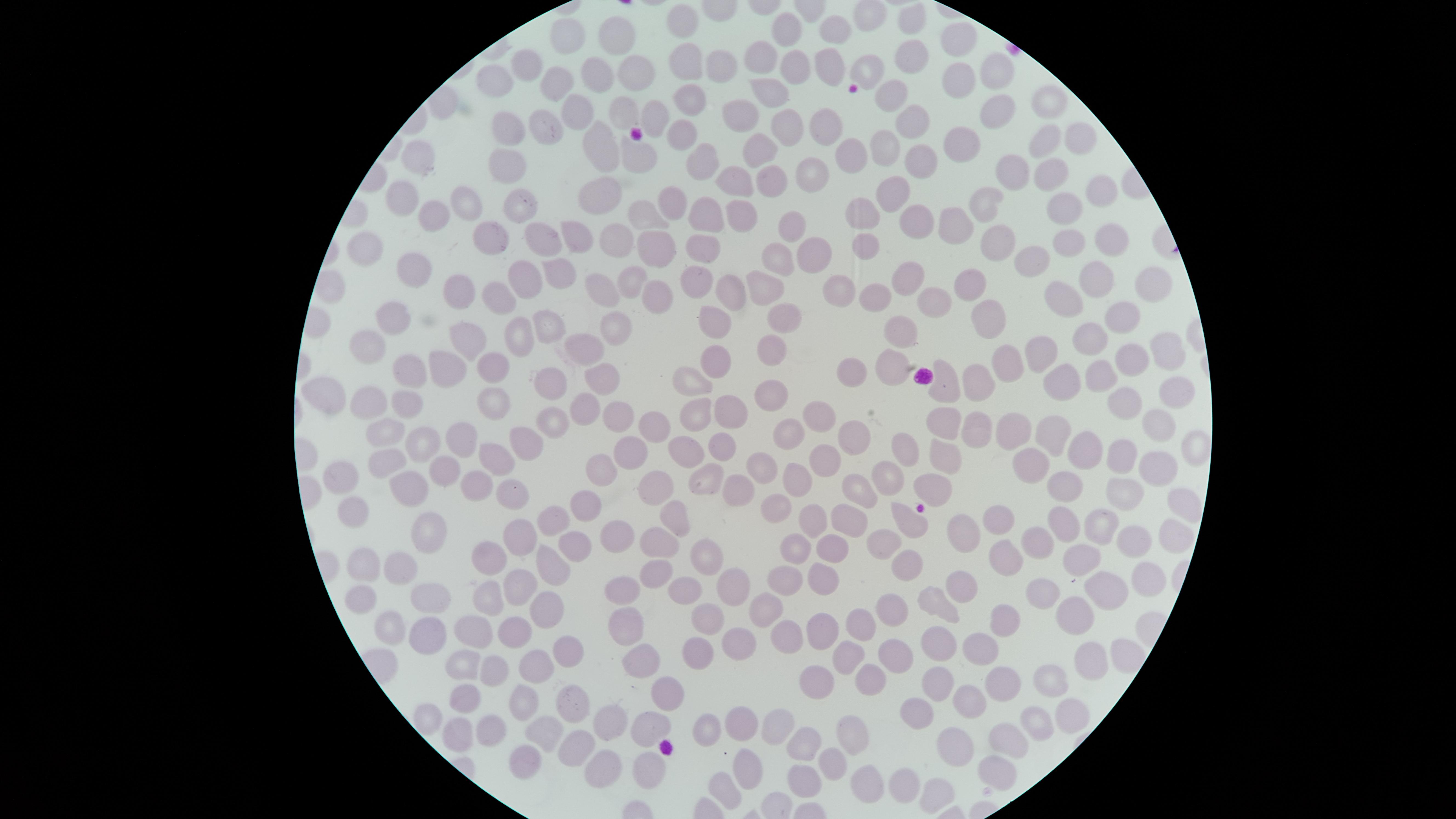
preparation = thin blood smear
image size = 1456×819 pixels
capture = smartphone photograph through the microscope eyepiece
presence = no malaria parasites detected
uninfected RBCs = approximate marker points as (x, y) in pixels: (875, 18), (908, 21), (787, 28), (840, 29), (685, 30), (622, 36), (571, 40), (959, 42), (903, 55), (759, 61), (526, 63), (824, 64), (859, 65), (689, 66), (790, 66), (721, 68), (631, 73), (998, 73), (955, 76), (496, 78), (598, 80), (558, 89), (760, 90), (892, 96), (689, 102), (1046, 103), (994, 111), (573, 114), (650, 115), (739, 116), (622, 117), (910, 120), (544, 123), (786, 124), (511, 127), (829, 129), (681, 134), (1076, 139), (962, 140), (1041, 140), (603, 143), (887, 148), (755, 154), (855, 154), (640, 156), (423, 157), (704, 157), (922, 159), (500, 165), (1012, 169), (815, 172), (1047, 172), (769, 177), (736, 180), (1102, 190), (893, 191), (603, 195), (405, 198), (469, 202), (982, 202), (675, 203), (519, 204), (1070, 206), (702, 210), (738, 213), (859, 213), (916, 218), (435, 219), (639, 222), (798, 223), (961, 223), (1107, 234), (584, 236), (1001, 237), (493, 238), (658, 238), (550, 239), (1069, 240), (866, 242), (618, 244), (705, 247), (365, 248), (812, 253), (777, 255), (1036, 256), (402, 267), (559, 274), (695, 277), (907, 277), (524, 278), (1090, 278), (632, 281), (1153, 283), (725, 284), (768, 284), (452, 285), (836, 287), (972, 287), (499, 290), (602, 290), (1058, 298), (649, 300), (935, 300), (873, 302), (782, 314), (994, 316), (1124, 316), (398, 318), (714, 319), (549, 323), (616, 326), (898, 331), (468, 332), (522, 333), (1096, 336), (769, 345), (365, 347), (587, 348), (1170, 348), (1055, 350), (718, 354), (1135, 356), (1010, 360), (493, 365), (851, 371), (415, 372), (447, 373), (894, 373), (1103, 373), (596, 375), (977, 375), (547, 383), (690, 383), (947, 384), (1064, 386), (1174, 387), (331, 392), (768, 394), (373, 401), (495, 402), (1119, 404), (407, 405), (585, 405), (695, 414), (734, 415), (813, 415), (1159, 416), (552, 421), (654, 426), (939, 430), (972, 432), (1009, 432), (393, 433), (1054, 434), (781, 435), (851, 438), (1194, 443), (429, 444), (524, 445), (463, 446), (1088, 447), (720, 449), (633, 452), (679, 452), (907, 452), (491, 456), (940, 458), (1121, 458), (822, 459), (386, 461), (1026, 461), (608, 462), (757, 466), (1155, 471), (440, 472), (892, 473), (702, 476), (339, 477), (796, 480), (1067, 481), (405, 483), (930, 484), (513, 485), (857, 485), (476, 488), (662, 491), (728, 491), (1122, 494), (591, 496), (776, 505), (1178, 508), (673, 513), (996, 515), (345, 517), (551, 518), (839, 519), (812, 521), (906, 522), (1095, 523), (1063, 525), (958, 529), (425, 531), (611, 531), (1038, 536), (1164, 536), (522, 537), (659, 537), (1129, 539), (573, 541), (831, 545), (887, 546), (796, 547), (999, 551), (491, 557), (704, 557), (1070, 561), (914, 562), (363, 566), (551, 566), (401, 568), (655, 573), (822, 574), (781, 577), (1144, 578), (516, 581), (725, 583), (956, 585), (617, 589), (681, 590), (1102, 590), (1045, 591), (434, 597), (488, 598), (361, 602), (547, 605), (761, 606), (887, 608), (937, 608), (709, 614), (1078, 618), (991, 619), (620, 621), (866, 623), (513, 625), (385, 630), (820, 632), (423, 633), (477, 633), (930, 639), (787, 641), (737, 643), (979, 645), (558, 650), (846, 651), (696, 653), (897, 653), (1091, 658), (459, 663), (531, 664), (644, 664), (498, 669), (934, 680), (999, 682), (1043, 682), (817, 685), (872, 685), (666, 693), (462, 696), (518, 700), (572, 700), (971, 700), (915, 708), (1073, 714), (1036, 724), (480, 728), (652, 728), (698, 728), (742, 728), (605, 729), (772, 729), (851, 729), (457, 731), (547, 736), (578, 739), (1014, 739), (805, 745), (961, 751), (643, 761), (523, 762), (748, 763), (825, 764), (602, 771), (997, 771), (866, 777), (901, 781), (802, 783), (727, 789), (939, 795)
visible region = circular
stain = Giemsa
field of view = single